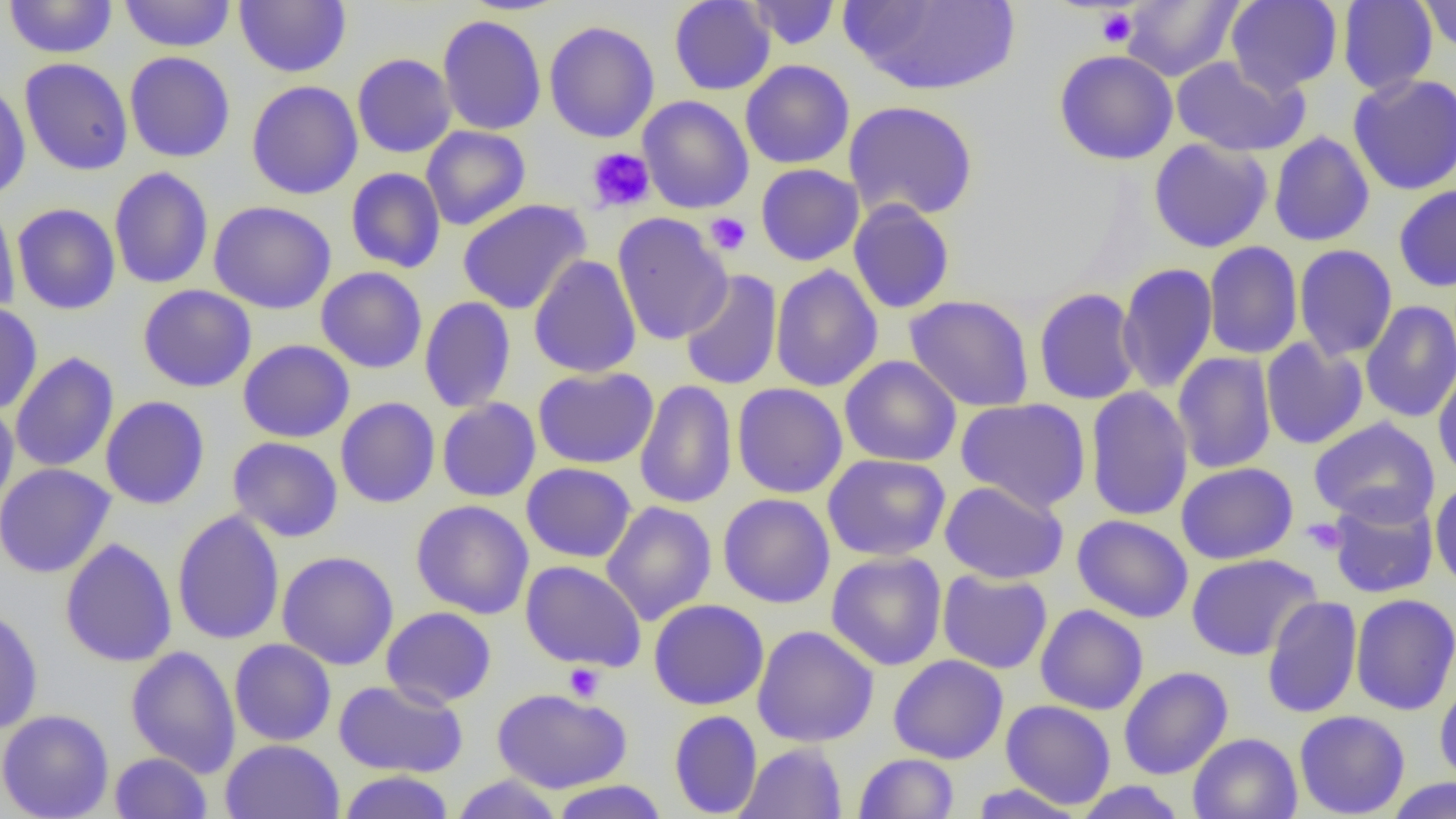
slide-level diagnosis = no evidence of blood parasites
uninfected red blood cell locations = approximate bounding boxes as [x1, y1, x2, y2] in pixels: [3, 0, 118, 58], [120, 0, 235, 52], [234, 0, 351, 78], [669, 0, 775, 96], [747, 0, 840, 50], [845, 0, 1021, 97], [1120, 0, 1243, 82], [1226, 0, 1342, 94], [1338, 0, 1438, 95], [1419, 0, 1456, 54], [438, 15, 547, 135], [544, 20, 659, 143], [1053, 50, 1178, 165], [124, 51, 236, 163], [352, 53, 457, 158], [1171, 55, 1309, 157], [19, 58, 133, 176], [740, 59, 855, 169], [1348, 73, 1456, 195], [0, 80, 31, 200], [246, 80, 363, 199], [637, 95, 753, 214], [843, 100, 979, 222], [421, 126, 531, 230], [1269, 131, 1375, 246], [1148, 138, 1274, 253], [755, 163, 864, 266], [109, 167, 213, 289], [345, 167, 446, 273], [1394, 185, 1456, 292], [458, 199, 591, 315], [848, 199, 956, 314], [0, 200, 20, 316], [209, 200, 336, 315], [12, 203, 121, 315], [612, 213, 732, 346], [1204, 241, 1303, 360], [1294, 244, 1397, 361], [529, 255, 641, 379], [1117, 262, 1218, 395], [770, 264, 884, 393], [316, 266, 427, 374], [679, 268, 783, 391], [138, 285, 256, 392], [1033, 288, 1142, 405], [904, 295, 1035, 412], [419, 296, 516, 413], [1360, 300, 1456, 423], [0, 302, 43, 416], [1260, 338, 1368, 450], [238, 339, 355, 442], [10, 352, 119, 473], [1172, 352, 1277, 474], [840, 355, 961, 466], [1433, 363, 1456, 484], [532, 366, 659, 469], [635, 379, 738, 509], [732, 382, 848, 499], [1085, 386, 1193, 521], [100, 395, 210, 510], [335, 397, 440, 508], [437, 398, 541, 502], [955, 398, 1091, 513], [0, 401, 19, 513], [1308, 417, 1440, 527], [228, 437, 343, 542], [822, 454, 951, 561], [521, 462, 636, 563], [1176, 462, 1298, 565], [0, 463, 116, 578], [940, 480, 1069, 584], [1430, 480, 1456, 593], [719, 493, 835, 608], [1327, 493, 1439, 599], [411, 499, 534, 619], [601, 501, 717, 625], [171, 510, 285, 645], [1072, 514, 1194, 623], [60, 538, 177, 667], [277, 551, 398, 670], [826, 551, 947, 670], [1185, 553, 1321, 661], [520, 560, 647, 671], [937, 569, 1052, 674], [1350, 593, 1456, 715], [1261, 595, 1363, 719], [648, 598, 769, 710], [1035, 604, 1149, 715], [0, 606, 44, 734], [381, 606, 497, 709], [752, 625, 879, 748], [229, 639, 337, 746], [126, 646, 241, 777], [888, 654, 1009, 764], [1118, 666, 1233, 780], [333, 679, 468, 777], [1434, 679, 1456, 786], [492, 688, 632, 794], [1001, 700, 1116, 809], [0, 709, 114, 819], [669, 710, 762, 818], [1294, 710, 1410, 818], [1188, 732, 1302, 819], [220, 739, 344, 819], [736, 742, 847, 818], [110, 752, 212, 818], [854, 753, 959, 818], [337, 770, 455, 818], [450, 774, 565, 818], [1384, 777, 1455, 818], [549, 780, 670, 818], [1073, 781, 1187, 818], [967, 783, 1087, 818]
preparation = thin blood film
modality = optical microscopy
image size = 1456×819 pixels
platelet locations = approximate bounding boxes as [x1, y1, x2, y2] in pixels: [1096, 8, 1137, 48], [587, 148, 655, 213], [705, 212, 751, 256], [1302, 518, 1347, 555], [564, 663, 605, 701]
magnification = 1000x
field of view = one of a larger specimen